Give the position of every malaria parasite.
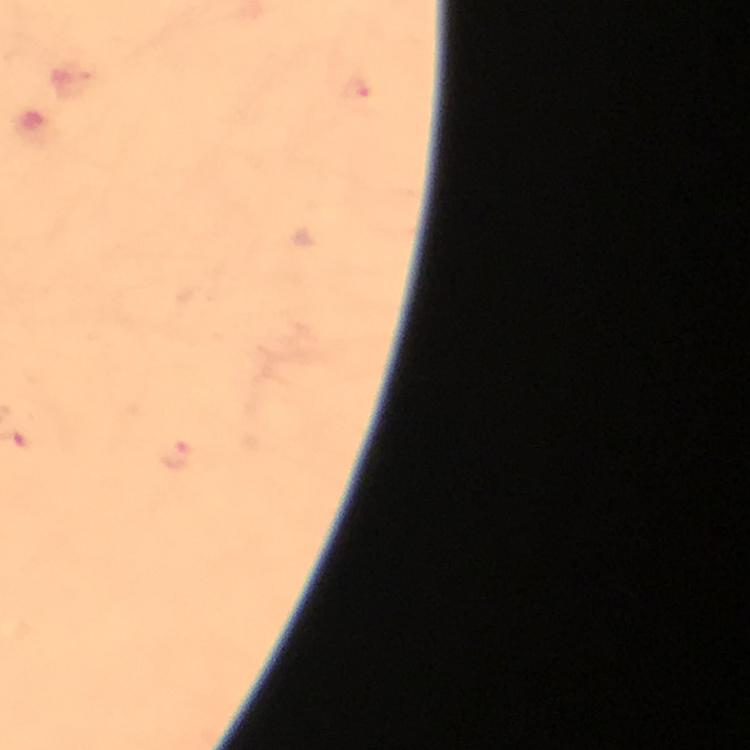
Approximate centers as [x, y] in pixels.
Malaria parasites: [355, 89], [174, 454].

From a malaria diagnostic workup. Image is 750×750 pixels. Immersion oil applied. 100x magnification. Cropped region of a single field of view. Thick blood film. Giemsa-stained preparation. Photographed with a smartphone mounted on the microscope.